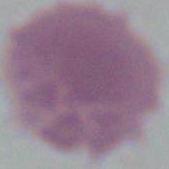

modality = photomicrograph
magnification = 1000x
identification = erythrocyte